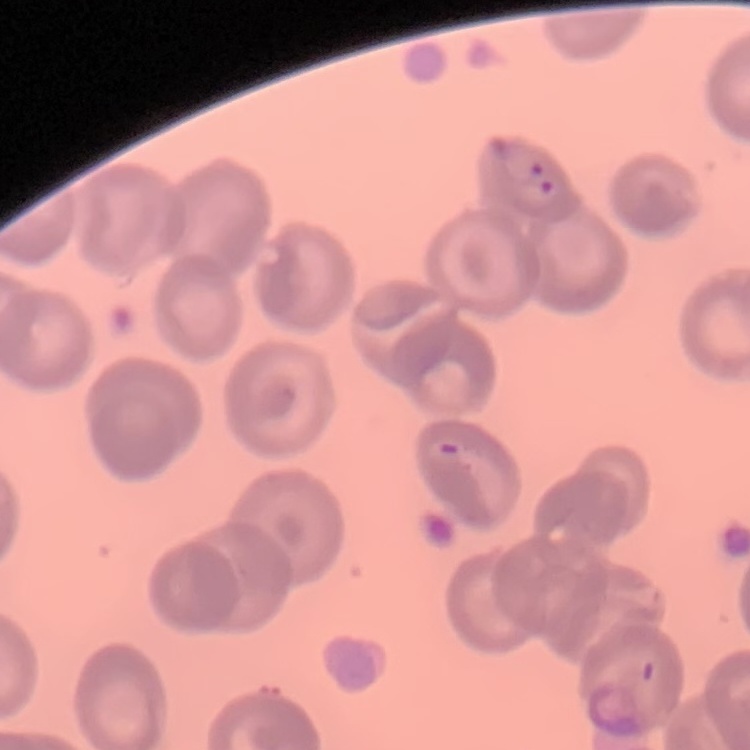
Summary:
  - Red blood cell morphology: no rouleaux formation
  - Preparation: thin peripheral smear
  - Stain: Field's or Giemsa
  - Image type: square crop of a larger photomicrograph